Locate every blood parasite and identify its species.
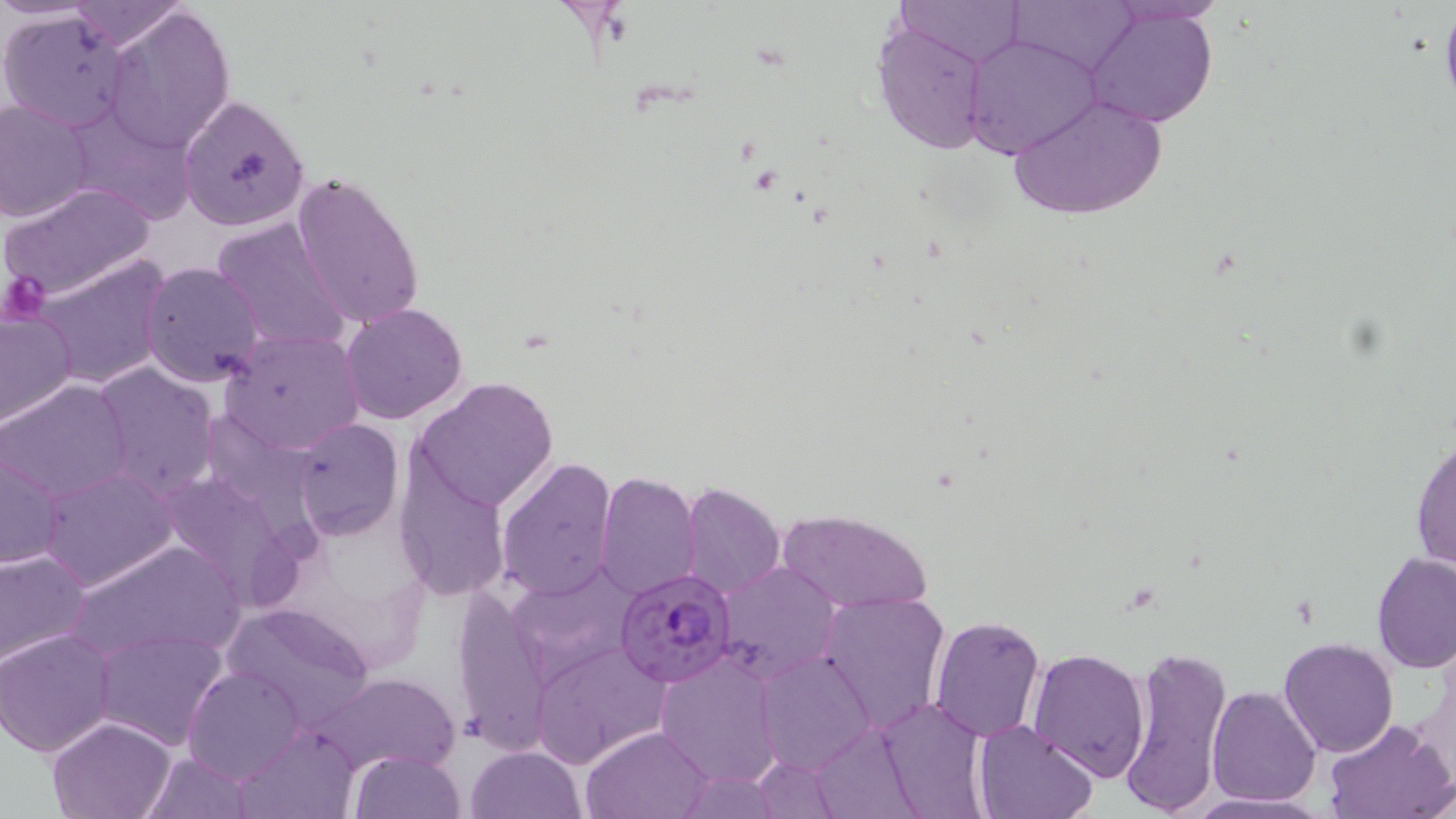
Approximate bounding boxes as (x1, y1, x2, y2) in pixels.
Plasmodium falciparum-infected red blood cells: (615, 566, 736, 688).
No Plasmodium ovale, Plasmodium malariae, Plasmodium vivax, Babesia divergens, or Trypanosoma brucei observed.

Platelet locations: (2, 269, 50, 321). Uninfected red blood cell locations: (897, 0, 1024, 67), (1010, 0, 1138, 77), (66, 1, 189, 51), (1113, 1, 1228, 25), (1085, 7, 1219, 130), (103, 8, 236, 154), (0, 11, 134, 132), (872, 21, 997, 156), (964, 34, 1098, 159), (1004, 93, 1169, 223), (177, 94, 310, 232), (0, 99, 94, 224), (64, 107, 199, 227), (291, 171, 426, 333), (0, 183, 157, 304), (210, 216, 351, 353), (31, 255, 170, 390), (140, 261, 266, 389), (340, 303, 469, 426), (0, 309, 77, 427), (221, 329, 366, 455), (90, 363, 219, 497), (413, 377, 558, 513), (3, 378, 134, 500), (291, 419, 405, 540), (1410, 433, 1455, 576), (1, 442, 68, 571), (496, 456, 618, 600), (391, 458, 512, 602), (35, 466, 179, 591), (151, 468, 305, 604), (594, 471, 701, 598), (679, 482, 784, 598), (776, 508, 931, 615), (63, 539, 245, 667), (0, 549, 92, 671), (1371, 553, 1456, 673), (716, 561, 840, 680), (817, 590, 950, 732), (451, 591, 551, 754), (222, 599, 376, 732), (930, 613, 1044, 742), (93, 628, 227, 749), (2, 629, 118, 755), (1280, 637, 1398, 757), (533, 644, 669, 768), (1116, 644, 1233, 819), (1027, 646, 1149, 781), (755, 649, 873, 774), (653, 653, 784, 788), (185, 666, 303, 782), (317, 674, 458, 773), (1207, 686, 1321, 806), (873, 699, 991, 816), (47, 716, 178, 819), (973, 719, 1096, 819), (1326, 719, 1456, 818), (236, 725, 360, 818), (582, 725, 711, 817), (466, 744, 584, 819), (348, 749, 467, 819), (141, 752, 255, 818). Slide-level diagnosis: Plasmodium falciparum. 1000x magnification. Optical microscopy. Single field of view. May-Grünwald-Giemsa stain. Image is 1456×819 pixels. Thin blood film.